Describe the morphology of the red blood cells.
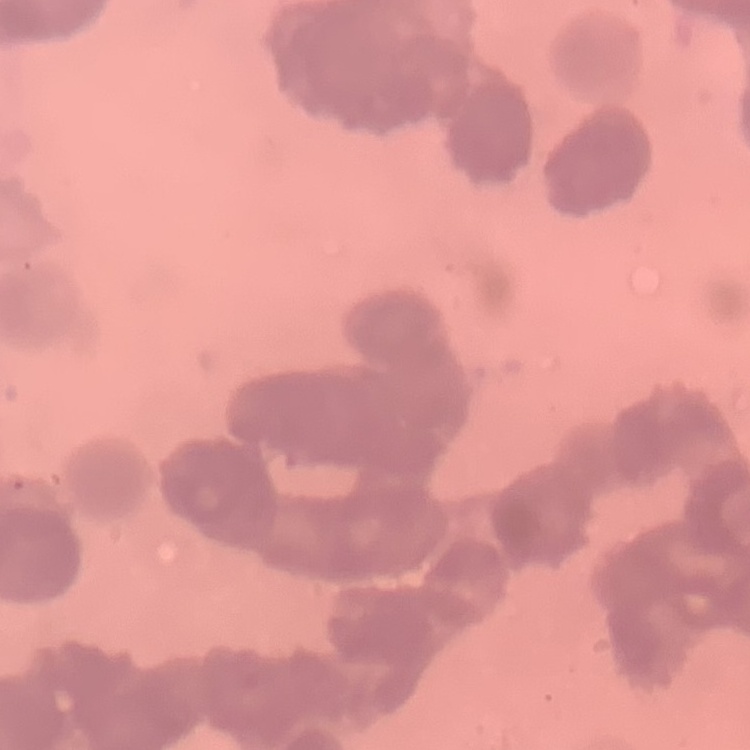
Rouleaux formation.

Summary:
  - Preparation: thin peripheral smear
  - Stain: Field's or Giemsa
  - Image type: one tile cut from a larger photomicrograph